Comment on the morphology of the erythrocytes.
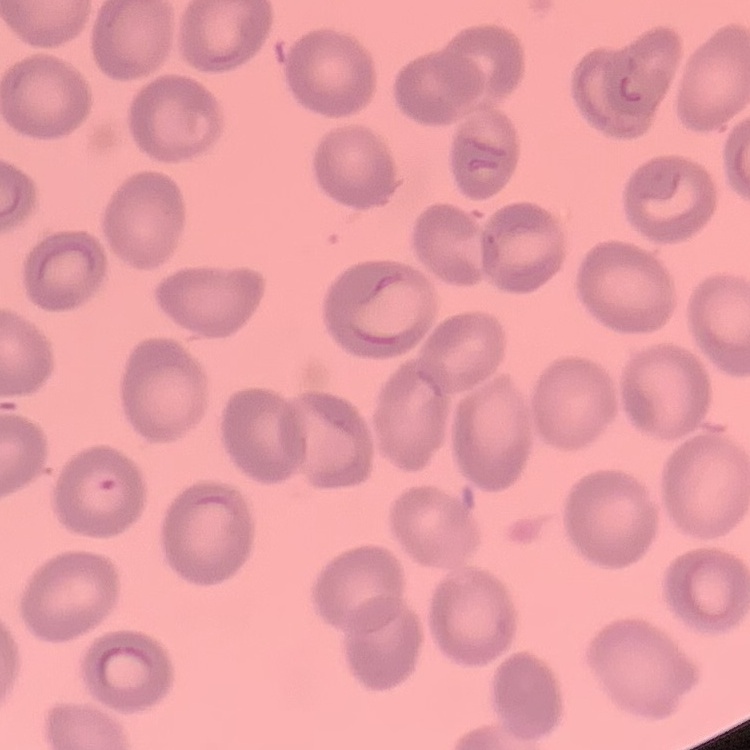

No rouleaux formation.

Summary:
  - Image type: square crop of a larger photomicrograph
  - Stain: Field's or Giemsa
  - Preparation: thin blood smear